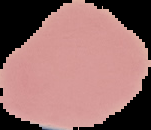 Image is 151×130 pixels. Malaria status: uninfected. From a thin blood film. Cell region segmented out of the field of view; the surrounding area is masked to black.